Classify this cell by malaria status.
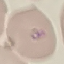
Parasitized.

Cell patch, automatically extracted from a larger field of view and resized to 64 × 64 pixels. Photographed with a smartphone camera at the microscope eyepiece. Giemsa-stained preparation. Thin blood smear.